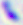
Summary:
  - Identification: Toxoplasma gondii
  - Magnification: 400x
  - Modality: photomicrograph